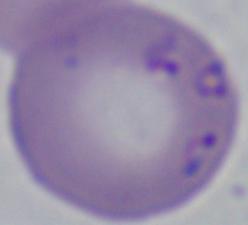
{
  "modality": "micrograph",
  "magnification": "1000x",
  "identification": "Babesia"
}